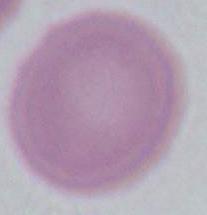 An erythrocyte is seen. Photomicrograph. Captured at 1000x magnification.